Assess for malaria.
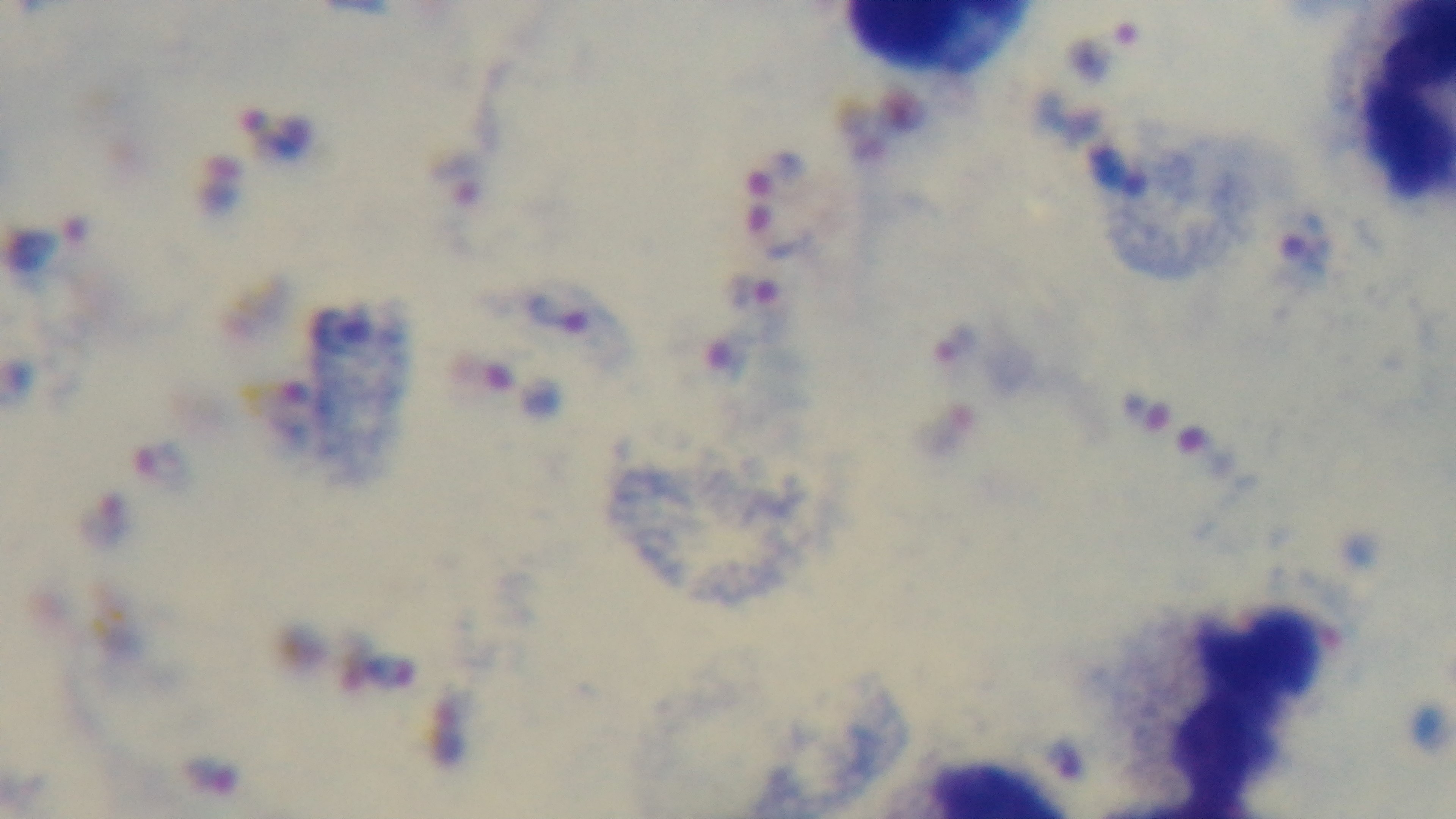

Positive.

Preparation: thick blood film. Mounted 4K digital camera. One field from the slide. Photomicrograph. Giemsa-stained. 100x oil-immersion objective.